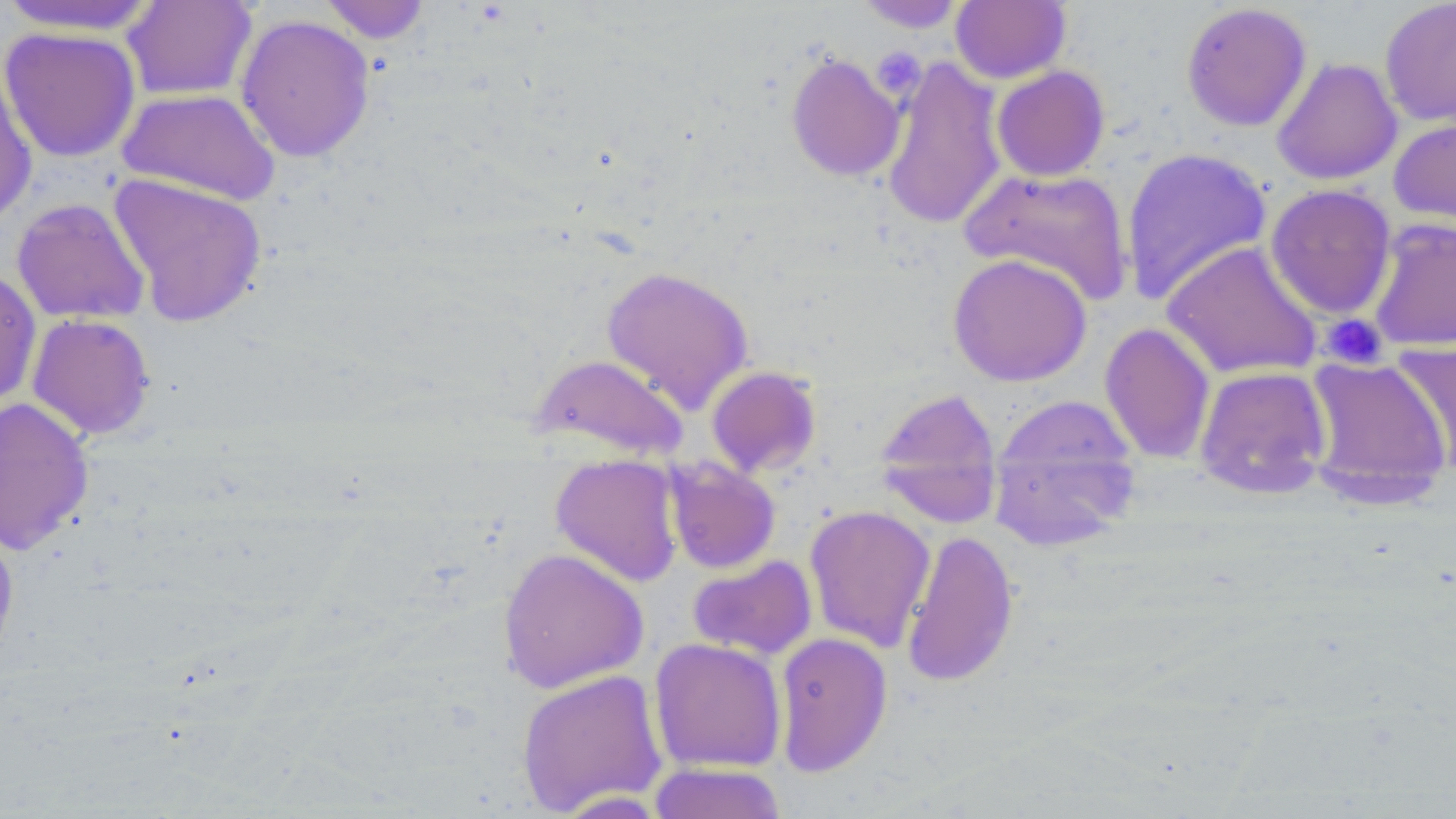
slide-level diagnosis = negative for blood parasites
field of view = single
modality = light microscopy
stain = May-Grünwald-Giemsa
platelet locations = approximate bounding boxes as named x1/y1/x2/y2 corners in pixels: (x1=871, y1=47, x2=926, y2=99), (x1=1321, y1=313, x2=1387, y2=369)
preparation = thin blood film
image size = 1456×819 pixels
uninfected red blood cell locations = approximate bounding boxes as named x1/y1/x2/y2 corners in pixels: (x1=121, y1=0, x2=258, y2=101), (x1=318, y1=0, x2=432, y2=43), (x1=950, y1=0, x2=1071, y2=84), (x1=0, y1=1, x2=163, y2=36), (x1=855, y1=1, x2=968, y2=33), (x1=1379, y1=1, x2=1456, y2=127), (x1=1181, y1=2, x2=1312, y2=132), (x1=236, y1=14, x2=375, y2=163), (x1=0, y1=27, x2=141, y2=163), (x1=785, y1=52, x2=906, y2=182), (x1=881, y1=57, x2=1006, y2=230), (x1=1272, y1=57, x2=1402, y2=185), (x1=0, y1=63, x2=37, y2=228), (x1=991, y1=66, x2=1110, y2=181), (x1=117, y1=88, x2=281, y2=206), (x1=1388, y1=116, x2=1456, y2=232), (x1=1120, y1=146, x2=1272, y2=305), (x1=959, y1=166, x2=1133, y2=306), (x1=108, y1=173, x2=268, y2=326), (x1=1264, y1=184, x2=1397, y2=319), (x1=12, y1=198, x2=150, y2=324), (x1=1367, y1=218, x2=1456, y2=352), (x1=1162, y1=241, x2=1322, y2=380), (x1=947, y1=253, x2=1092, y2=386), (x1=600, y1=265, x2=754, y2=414), (x1=0, y1=268, x2=41, y2=409), (x1=26, y1=313, x2=155, y2=440), (x1=1099, y1=322, x2=1216, y2=464), (x1=1392, y1=338, x2=1456, y2=474), (x1=529, y1=353, x2=689, y2=461), (x1=1303, y1=356, x2=1452, y2=505), (x1=706, y1=365, x2=821, y2=477), (x1=1194, y1=365, x2=1332, y2=500), (x1=873, y1=387, x2=1003, y2=528), (x1=988, y1=396, x2=1141, y2=549), (x1=0, y1=397, x2=93, y2=555), (x1=550, y1=453, x2=684, y2=587), (x1=665, y1=458, x2=781, y2=573), (x1=804, y1=504, x2=936, y2=653), (x1=0, y1=521, x2=20, y2=671), (x1=900, y1=528, x2=1019, y2=688), (x1=497, y1=547, x2=649, y2=694), (x1=687, y1=555, x2=817, y2=660), (x1=773, y1=632, x2=893, y2=776), (x1=649, y1=637, x2=787, y2=773), (x1=516, y1=668, x2=668, y2=816), (x1=647, y1=762, x2=788, y2=819)
magnification = 1000x